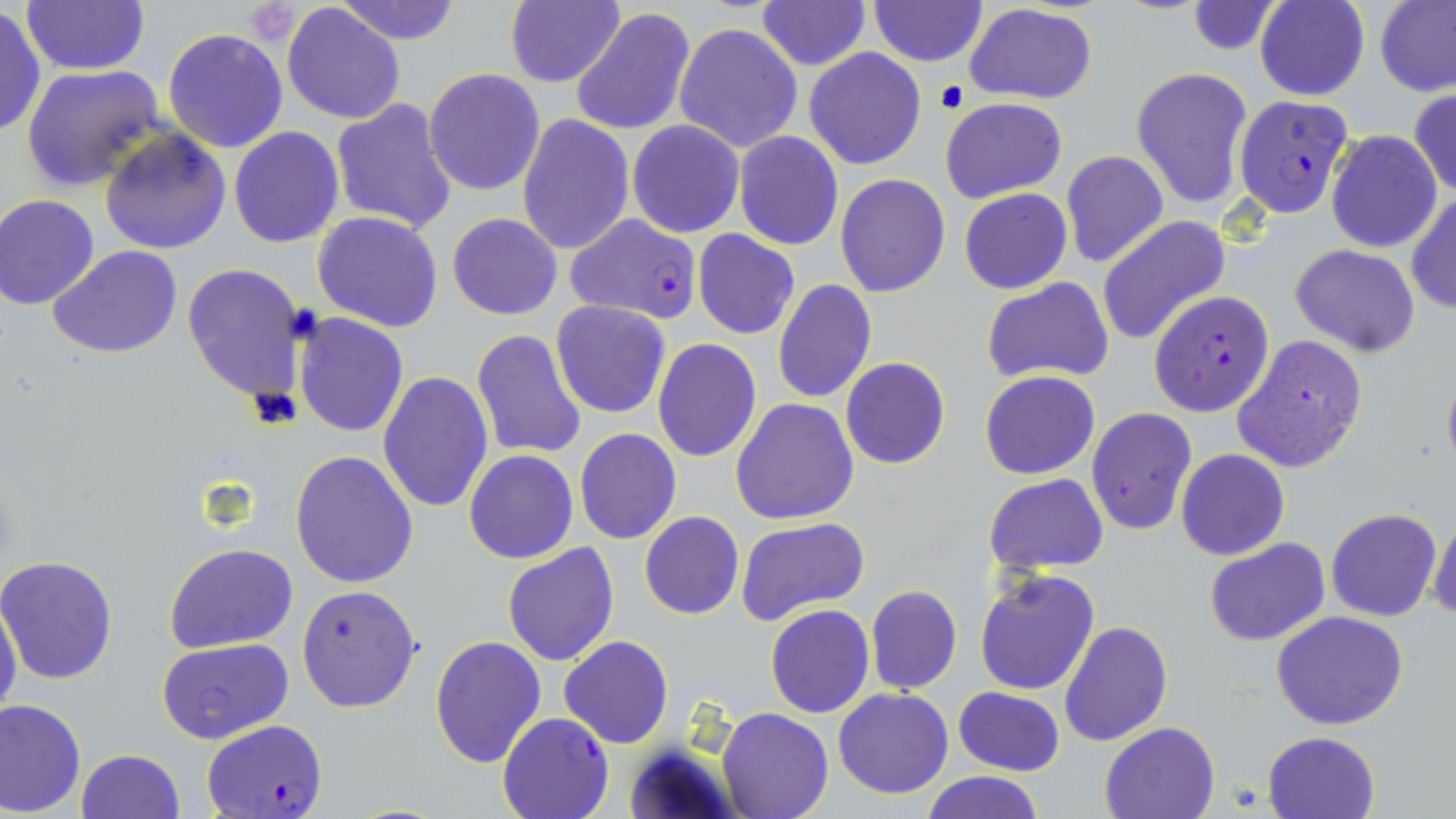

Summary:
  - Coordinate format: approximate bounding boxes as (x1,y1)-(x2,y2) corner pairs in pixels
  - Platelet locations: (245,0)-(301,46)
  - Plasmodium falciparum-infected red blood cell locations: (1234,94)-(1355,217), (563,214)-(703,323), (1147,290)-(1275,417), (497,711)-(614,819), (203,720)-(328,818)
  - Uninfected red blood cell locations: (20,0)-(147,74), (332,0)-(465,44), (754,0)-(870,71), (868,0)-(985,66), (1256,0)-(1369,101), (1375,0)-(1456,97), (504,1)-(626,88), (1186,2)-(1282,56), (281,3)-(407,127), (965,4)-(1095,103), (569,6)-(694,139), (0,7)-(45,141), (673,22)-(803,154), (162,27)-(290,154), (804,48)-(925,169), (20,64)-(165,190), (1130,66)-(1253,211), (423,69)-(545,194), (1408,89)-(1456,198), (939,97)-(1067,204), (330,99)-(456,233), (518,113)-(634,257), (628,120)-(744,238), (229,126)-(344,248), (100,127)-(231,255), (1326,129)-(1442,252), (734,132)-(843,250), (1060,150)-(1169,268), (834,173)-(952,297), (958,188)-(1072,294), (1407,192)-(1456,315), (0,194)-(101,310), (313,211)-(442,332), (447,212)-(563,321), (1097,216)-(1232,346), (693,230)-(800,340), (1290,244)-(1421,357), (49,246)-(185,361), (182,262)-(309,406), (981,277)-(1114,384), (774,279)-(876,403), (551,300)-(672,419), (293,313)-(408,438), (471,329)-(587,461), (1232,333)-(1368,474), (653,339)-(761,463), (841,357)-(949,469), (377,370)-(491,514), (979,371)-(1100,480), (731,397)-(859,523), (1087,408)-(1197,538), (574,428)-(682,546), (290,449)-(420,589), (465,449)-(578,564), (1176,449)-(1290,561), (984,474)-(1110,574), (1326,508)-(1442,622), (1427,510)-(1456,623), (639,511)-(744,620), (735,516)-(872,627), (1204,539)-(1330,647), (501,541)-(619,667), (165,543)-(296,653), (0,556)-(120,685), (975,567)-(1100,696), (296,585)-(422,714), (865,585)-(962,695), (0,591)-(23,730), (765,605)-(875,719), (1270,610)-(1410,731), (1060,621)-(1172,748), (428,634)-(547,767), (558,636)-(673,749), (156,638)-(293,744), (955,686)-(1065,777), (833,688)-(955,798), (0,698)-(86,815), (717,705)-(833,819), (1100,721)-(1222,818), (1262,730)-(1381,819), (77,749)-(185,819), (920,773)-(1045,819)
  - Slide-level diagnosis: Plasmodium falciparum
  - Field of view: one of a larger specimen
  - Modality: light microscopy
  - Magnification: 1000x
  - Preparation: thin blood smear
  - Stain: May-Grünwald-Giemsa
  - Image size: 1456×819 pixels